Assess the background quality.
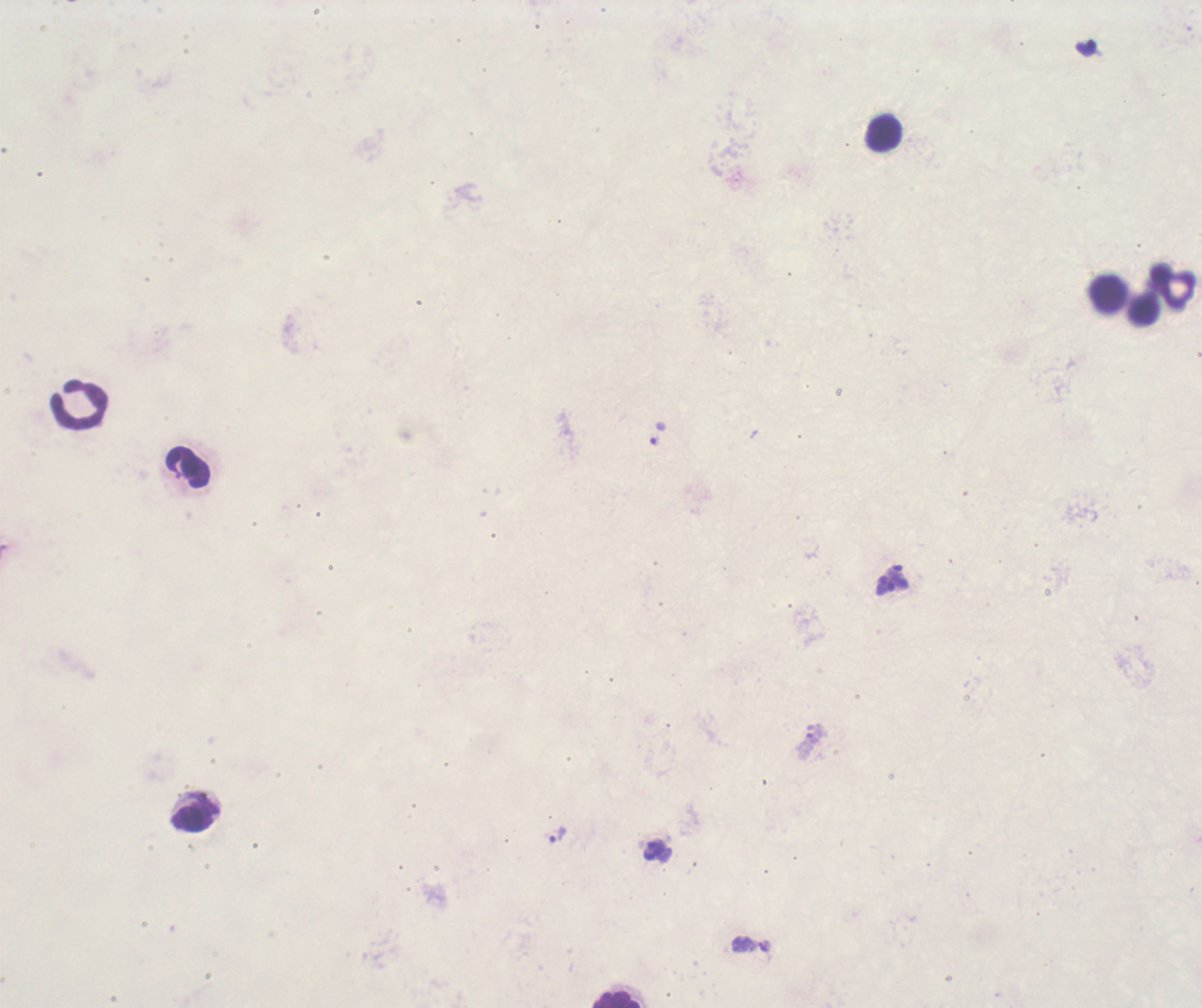
Unsatisfactory.

Approximate centers as (x, y) in pixels. Leukocyte locations: (882, 132), (1172, 287), (1106, 294), (1141, 310), (78, 404), (188, 468), (195, 812), (617, 1000). Trophozoite locations: (558, 835). Previously used in a real diagnosis. Image is 1202×1008 pixels. Thick blood film. Romanowsky stain. Coloration quality: bad. Result: malaria parasites identified. Single field of view. Captured at 100x magnification.